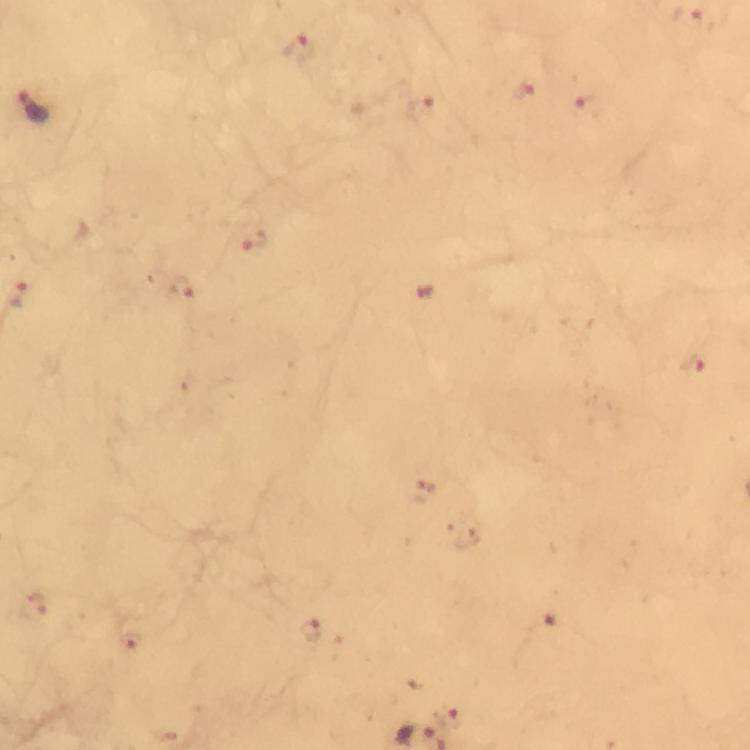
Approximate object centers, in pixels from the top-left corner.
Summary:
  - Malaria parasite locations: (x=691, y=24), (x=297, y=49), (x=524, y=92), (x=34, y=105), (x=592, y=105), (x=426, y=108), (x=253, y=242), (x=184, y=289), (x=427, y=292), (x=694, y=361), (x=424, y=491), (x=466, y=539), (x=38, y=605), (x=311, y=628), (x=129, y=641), (x=447, y=714)
  - Context: from a diagnostic examination for malaria
  - Capture: smartphone photograph through a microscope
  - Preparation: thick smear
  - Stain: Giemsa
  - Immersion oil: applied
  - Image size: 750×750 pixels
  - Magnification: 100x
  - Cropped from: a single field of view